Locate every blood parasite and identify its species.
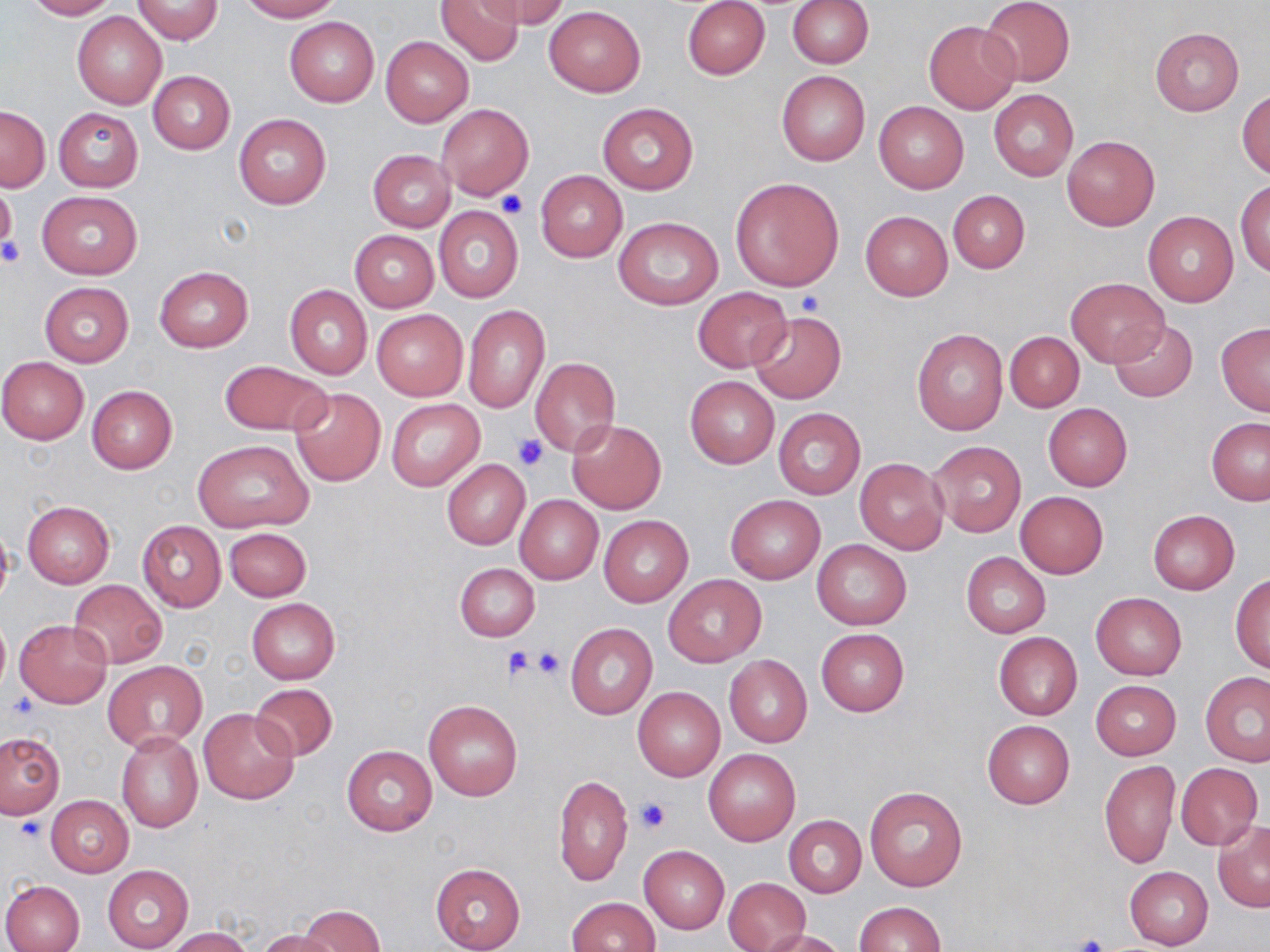

No blood parasites seen.

Approximate bounding boxes as named x1/y1/x2/y2 corners in pixels. Platelet locations: (x1=498, y1=189, x2=527, y2=218), (x1=1, y1=238, x2=25, y2=265), (x1=798, y1=292, x2=827, y2=315), (x1=512, y1=434, x2=548, y2=472), (x1=504, y1=647, x2=536, y2=681), (x1=533, y1=647, x2=566, y2=678), (x1=4, y1=694, x2=38, y2=724), (x1=634, y1=798, x2=671, y2=832), (x1=14, y1=816, x2=48, y2=843), (x1=1073, y1=934, x2=1110, y2=952). Uninfected red blood cell locations: (x1=23, y1=0, x2=117, y2=20), (x1=133, y1=0, x2=223, y2=44), (x1=241, y1=0, x2=340, y2=21), (x1=434, y1=0, x2=523, y2=66), (x1=479, y1=0, x2=571, y2=27), (x1=980, y1=0, x2=1076, y2=87), (x1=682, y1=1, x2=770, y2=79), (x1=788, y1=1, x2=873, y2=69), (x1=545, y1=6, x2=646, y2=96), (x1=72, y1=11, x2=167, y2=110), (x1=284, y1=17, x2=379, y2=106), (x1=924, y1=20, x2=1020, y2=113), (x1=1150, y1=27, x2=1243, y2=115), (x1=381, y1=36, x2=473, y2=126), (x1=776, y1=70, x2=870, y2=166), (x1=149, y1=72, x2=234, y2=153), (x1=989, y1=89, x2=1078, y2=181), (x1=1236, y1=90, x2=1269, y2=179), (x1=874, y1=101, x2=968, y2=193), (x1=597, y1=102, x2=698, y2=195), (x1=437, y1=103, x2=534, y2=199), (x1=1, y1=106, x2=49, y2=191), (x1=54, y1=107, x2=143, y2=192), (x1=234, y1=113, x2=331, y2=210), (x1=1061, y1=136, x2=1159, y2=231), (x1=369, y1=149, x2=456, y2=231), (x1=362, y1=150, x2=446, y2=308), (x1=536, y1=170, x2=627, y2=261), (x1=729, y1=177, x2=845, y2=291), (x1=1236, y1=179, x2=1270, y2=278), (x1=0, y1=184, x2=17, y2=250), (x1=948, y1=189, x2=1029, y2=273), (x1=37, y1=190, x2=142, y2=279), (x1=434, y1=206, x2=524, y2=302), (x1=1142, y1=210, x2=1239, y2=307), (x1=860, y1=211, x2=952, y2=299), (x1=614, y1=216, x2=723, y2=311), (x1=350, y1=230, x2=439, y2=312), (x1=155, y1=266, x2=252, y2=352), (x1=1065, y1=277, x2=1167, y2=366), (x1=39, y1=282, x2=134, y2=366), (x1=285, y1=285, x2=372, y2=379), (x1=693, y1=287, x2=793, y2=372), (x1=463, y1=305, x2=550, y2=413), (x1=370, y1=307, x2=467, y2=401), (x1=746, y1=310, x2=847, y2=405), (x1=1109, y1=319, x2=1199, y2=403), (x1=1215, y1=323, x2=1270, y2=415), (x1=911, y1=329, x2=1009, y2=436), (x1=1005, y1=332, x2=1084, y2=411), (x1=0, y1=357, x2=89, y2=444), (x1=530, y1=358, x2=621, y2=457), (x1=220, y1=360, x2=330, y2=436), (x1=685, y1=375, x2=778, y2=469), (x1=87, y1=385, x2=177, y2=474), (x1=288, y1=387, x2=386, y2=486), (x1=387, y1=398, x2=486, y2=492), (x1=1042, y1=403, x2=1133, y2=492), (x1=773, y1=406, x2=866, y2=500), (x1=1206, y1=418, x2=1270, y2=505), (x1=568, y1=420, x2=665, y2=515), (x1=193, y1=439, x2=314, y2=535), (x1=929, y1=441, x2=1026, y2=537), (x1=854, y1=458, x2=948, y2=553), (x1=441, y1=459, x2=529, y2=549), (x1=1015, y1=491, x2=1108, y2=578), (x1=515, y1=495, x2=603, y2=583), (x1=725, y1=495, x2=825, y2=583), (x1=22, y1=501, x2=114, y2=587), (x1=1148, y1=510, x2=1240, y2=594), (x1=598, y1=514, x2=692, y2=607), (x1=0, y1=518, x2=14, y2=610), (x1=136, y1=520, x2=226, y2=612), (x1=224, y1=527, x2=312, y2=601), (x1=812, y1=538, x2=912, y2=629), (x1=961, y1=551, x2=1050, y2=637), (x1=455, y1=562, x2=540, y2=641), (x1=664, y1=574, x2=765, y2=666), (x1=1230, y1=574, x2=1270, y2=673), (x1=69, y1=579, x2=166, y2=669), (x1=1091, y1=592, x2=1187, y2=680), (x1=246, y1=598, x2=340, y2=683), (x1=0, y1=615, x2=10, y2=691), (x1=13, y1=620, x2=112, y2=707), (x1=565, y1=622, x2=658, y2=720), (x1=816, y1=628, x2=908, y2=716), (x1=994, y1=632, x2=1082, y2=720), (x1=724, y1=654, x2=812, y2=748), (x1=103, y1=661, x2=208, y2=751), (x1=1200, y1=671, x2=1270, y2=766), (x1=1091, y1=680, x2=1181, y2=760), (x1=249, y1=683, x2=338, y2=761), (x1=632, y1=687, x2=725, y2=781), (x1=424, y1=699, x2=522, y2=800), (x1=199, y1=708, x2=299, y2=805), (x1=982, y1=719, x2=1074, y2=809), (x1=116, y1=731, x2=203, y2=832), (x1=0, y1=733, x2=64, y2=817), (x1=341, y1=745, x2=437, y2=835), (x1=704, y1=748, x2=800, y2=845), (x1=1099, y1=760, x2=1180, y2=869), (x1=1176, y1=763, x2=1263, y2=849), (x1=554, y1=774, x2=632, y2=887), (x1=863, y1=785, x2=968, y2=892), (x1=45, y1=795, x2=133, y2=878), (x1=783, y1=814, x2=867, y2=897), (x1=1211, y1=821, x2=1270, y2=912), (x1=640, y1=845, x2=729, y2=932), (x1=430, y1=863, x2=525, y2=951), (x1=102, y1=865, x2=192, y2=952), (x1=1124, y1=866, x2=1212, y2=949), (x1=723, y1=877, x2=809, y2=951), (x1=1, y1=879, x2=84, y2=952), (x1=567, y1=896, x2=659, y2=951), (x1=853, y1=902, x2=945, y2=951), (x1=297, y1=904, x2=387, y2=952), (x1=166, y1=928, x2=252, y2=952), (x1=758, y1=928, x2=847, y2=952), (x1=257, y1=929, x2=345, y2=952). Slide-level diagnosis: negative for blood parasites. Image is 1270×952 pixels. May-Grünwald-Giemsa stain. Thin blood smear. Optical microscopy. Captured at 1000x magnification. One field of a larger specimen.